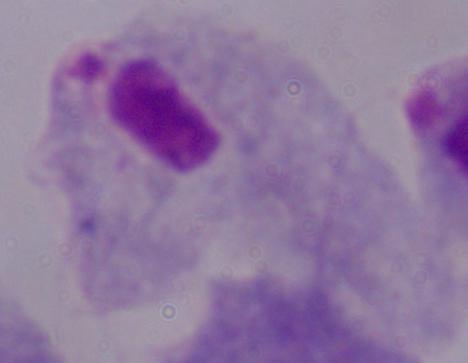

{
  "magnification": "1000x",
  "modality": "micrograph",
  "identification": "trichomonad"
}